Report the malaria status of this cell.
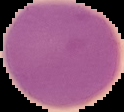

It is uninfected.

{
  "image_size": "124×112 pixels",
  "image_type": "cell region segmented out of the field of view; surrounding area masked to black",
  "preparation": "thin blood film"
}